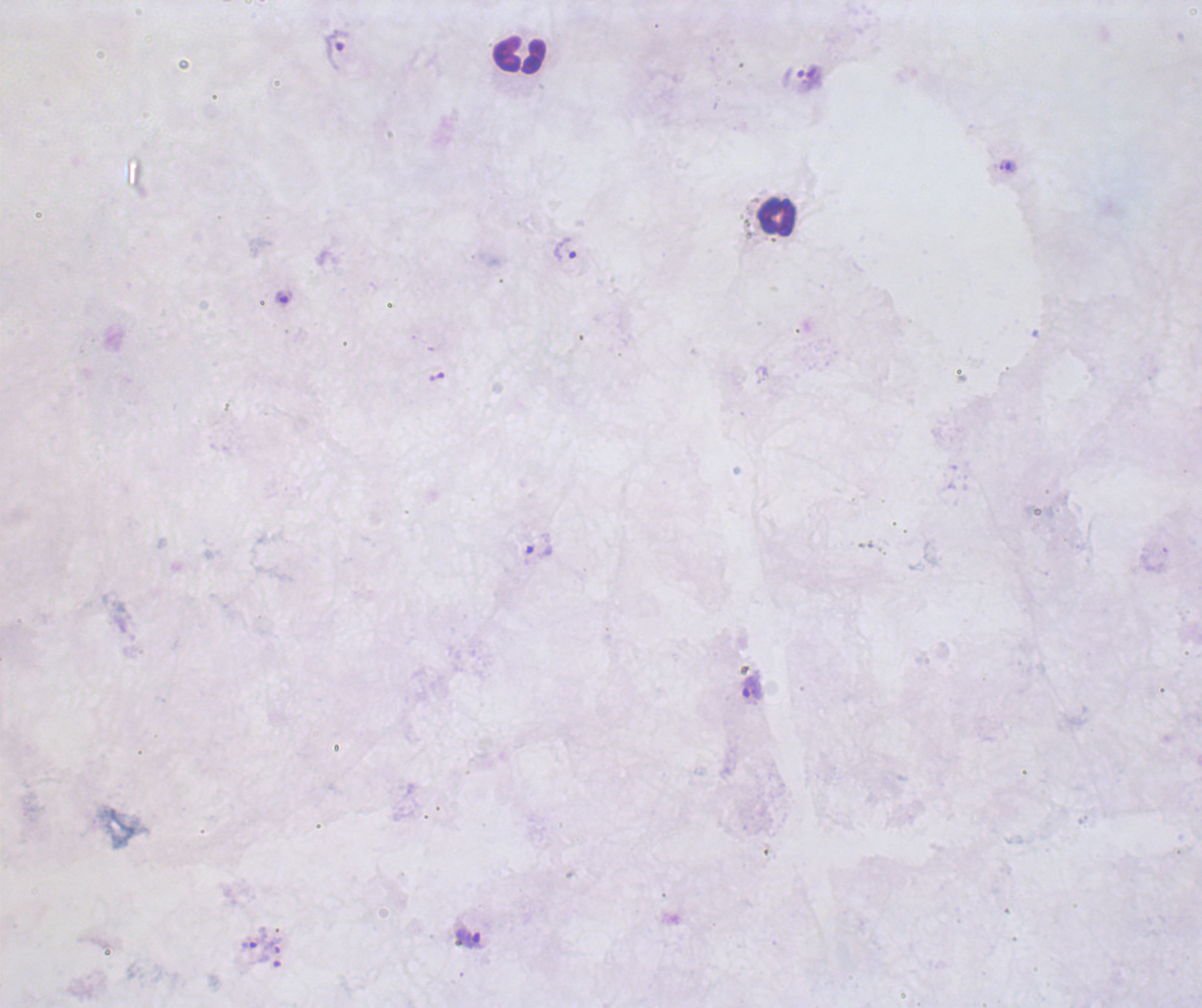

Approximate object centers, in pixels from the top-left corner. Leukocyte locations: (x=519, y=54), (x=777, y=217). Trophozoite locations: (x=337, y=50), (x=567, y=248), (x=283, y=298), (x=539, y=544), (x=753, y=688), (x=252, y=938), (x=470, y=939). Romanowsky-stained preparation. Captured at 100x magnification. Result: Plasmodium parasites identified. Image is 1202×1008 pixels. Previously used in a real diagnosis. One field from this slide. Coloration quality: bad. Background quality: unsatisfactory. Thick blood smear.